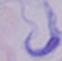
modality = micrograph
magnification = 1000x
identification = trypanosome